Name the blood parasite species.
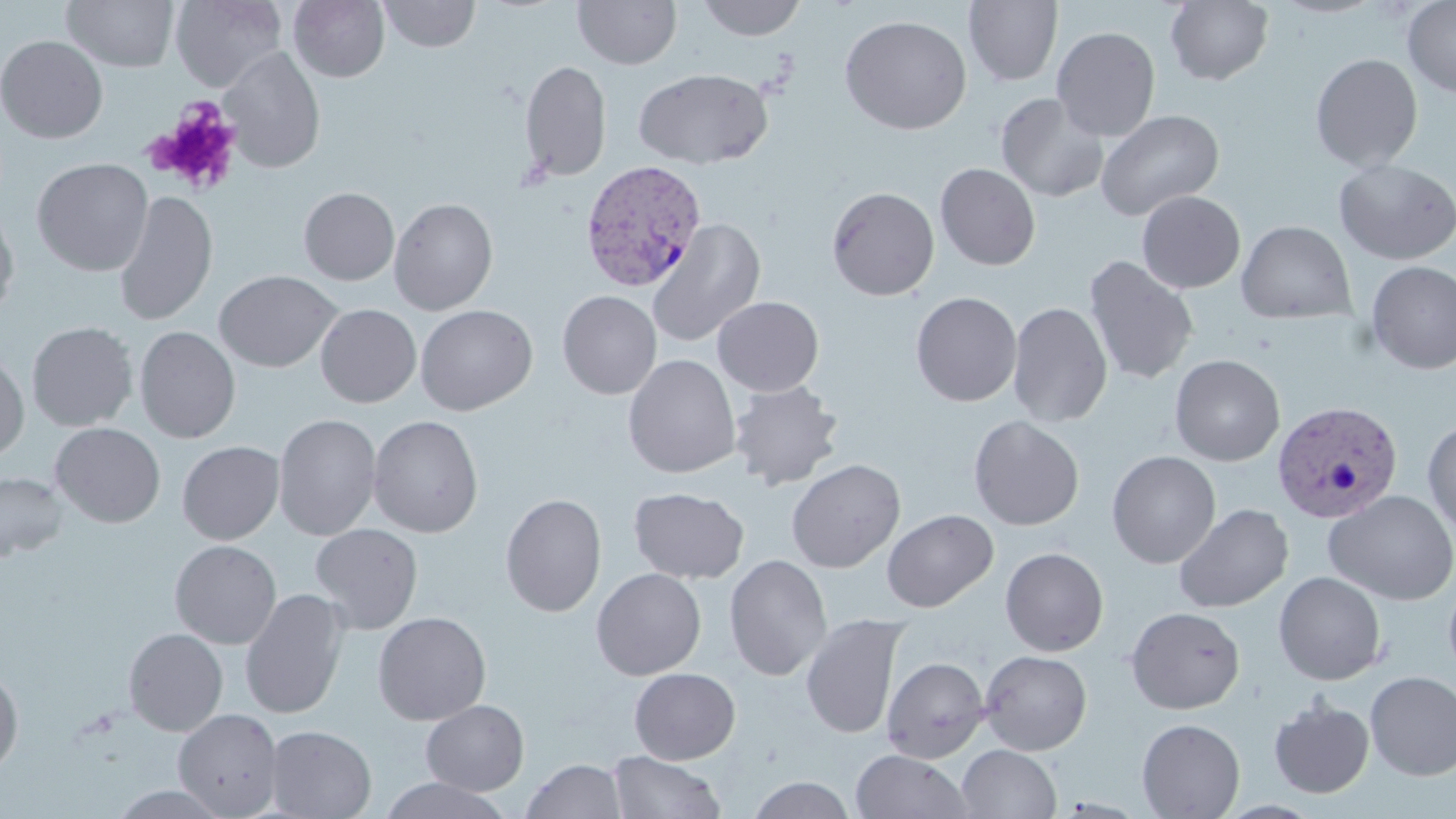

Plasmodium vivax.

Summary:
  - Coordinate format: approximate bounding boxes as (x1,y1)-(x2,y2) corner pairs in pixels
  - Uninfected red blood cell locations: (62,0)-(180,72), (170,0)-(288,91), (288,0)-(390,82), (378,0)-(480,52), (573,0)-(682,69), (698,0)-(806,41), (964,0)-(1062,86), (1165,0)-(1274,85), (1402,0)-(1456,97), (839,15)-(973,135), (1052,26)-(1161,141), (0,35)-(108,143), (218,46)-(325,173), (1310,53)-(1423,172), (518,60)-(612,182), (635,68)-(772,169), (995,92)-(1109,203), (1095,109)-(1225,221), (31,157)-(154,276), (1334,159)-(1456,265), (935,162)-(1041,270), (826,186)-(940,301), (299,187)-(400,285), (113,190)-(218,326), (1136,190)-(1245,294), (389,197)-(498,315), (0,203)-(19,322), (647,218)-(766,347), (1236,220)-(1356,324), (1083,255)-(1199,385), (1366,261)-(1456,375), (214,270)-(341,372), (557,290)-(661,399), (911,291)-(1022,407), (712,296)-(824,396), (1007,302)-(1112,427), (315,304)-(421,408), (415,304)-(538,415), (26,321)-(138,431), (134,326)-(241,444), (0,351)-(29,462), (623,354)-(740,478), (1170,354)-(1285,466), (728,380)-(844,490), (273,413)-(382,541), (367,415)-(484,538), (968,415)-(1085,530), (1422,419)-(1456,541), (50,422)-(165,528), (177,441)-(284,544), (1106,450)-(1221,569), (787,459)-(905,573), (0,471)-(68,562), (629,487)-(749,583), (1324,491)-(1456,605), (499,494)-(607,617), (1173,503)-(1294,613), (882,509)-(998,612), (310,523)-(424,635), (170,540)-(282,649), (1000,547)-(1109,656), (724,554)-(832,680), (591,568)-(706,680), (1443,570)-(1456,682), (1273,571)-(1387,685), (239,589)-(350,719), (1125,606)-(1246,714), (372,612)-(491,725), (800,614)-(907,739), (123,628)-(228,736), (979,650)-(1093,755), (882,656)-(990,762), (0,667)-(24,778), (629,668)-(740,764), (1365,671)-(1456,780), (1268,696)-(1375,798), (421,700)-(529,796), (173,708)-(284,818), (1136,718)-(1245,818), (264,725)-(377,818), (957,744)-(1062,819), (851,749)-(975,818), (608,750)-(726,818), (522,758)-(627,818), (747,775)-(856,818), (378,777)-(512,818), (108,786)-(233,819)
  - Platelet locations: (150,99)-(243,195)
  - Plasmodium vivax-infected red blood cell locations: (579,159)-(707,292), (1272,401)-(1403,523)
  - Field of view: single
  - Image size: 1456×819 pixels
  - Magnification: 1000x
  - Stain: May-Grünwald-Giemsa
  - Modality: light microscopy
  - Preparation: thin blood smear